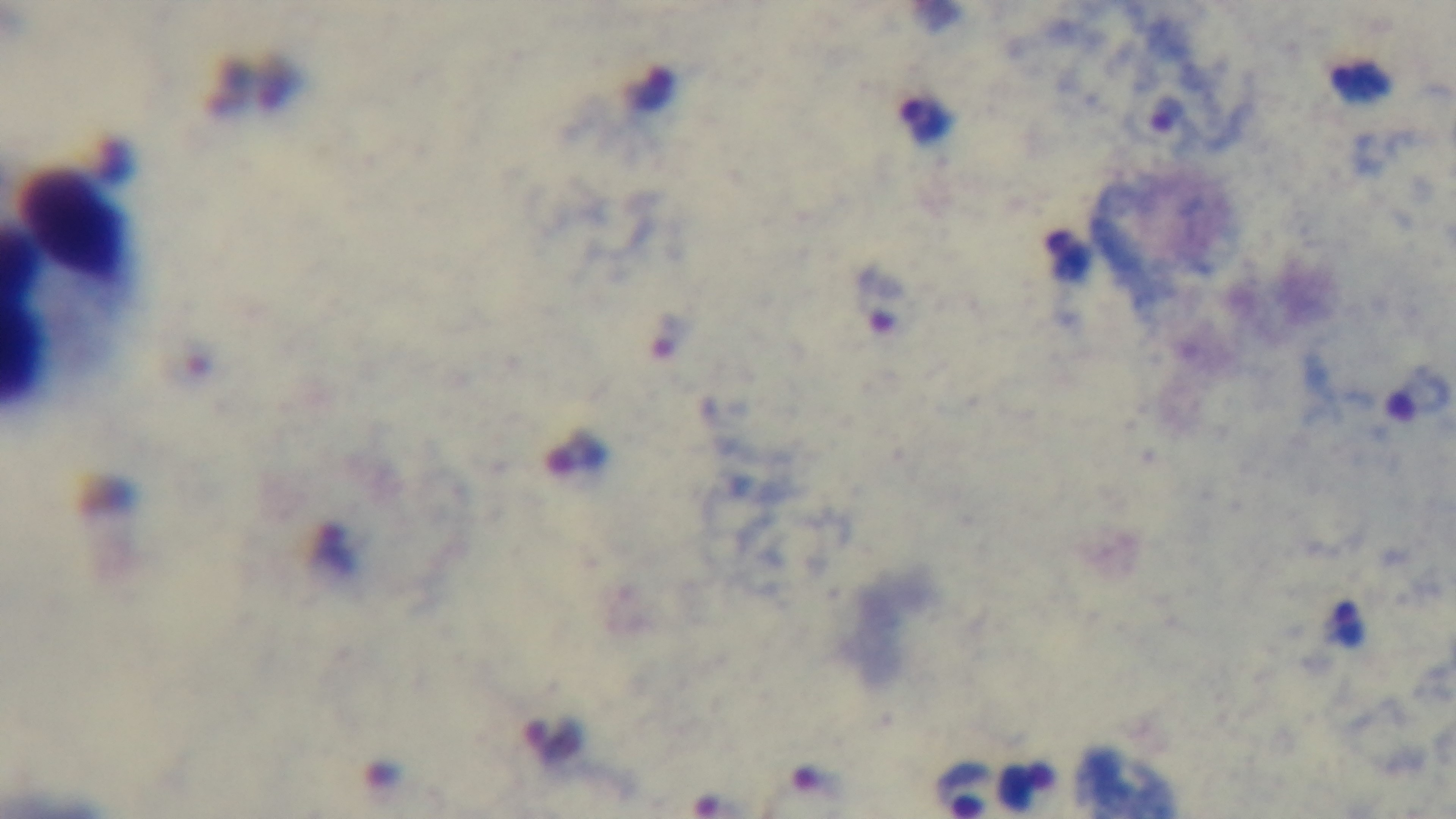

Summary:
  - Modality: light microscopy
  - Capture: mounted 4K digital camera
  - Field of view: one from the slide
  - Stain: Giemsa
  - Preparation: thick
  - Objective: 100x oil immersion
  - Malaria status: infected